Classify this cell by malaria status.
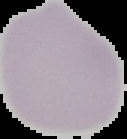

It is uninfected.

image type = segmented cell region with the area outside set to black
preparation = thin blood smear
image size = 127×139 pixels